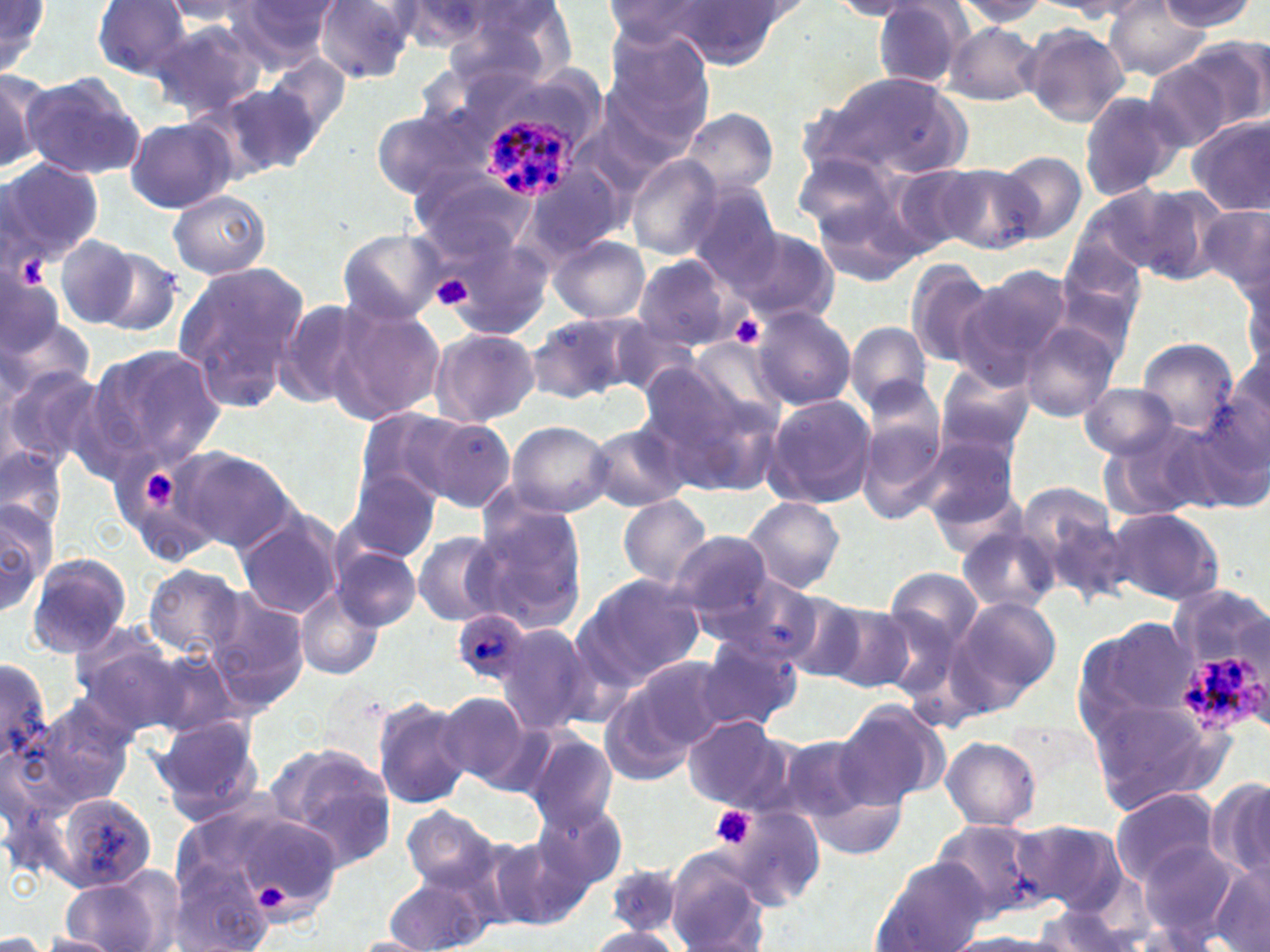
Approximate bounding boxes as (x1, y1, x2, y2) in pixels. Platelet locations: (432, 273, 473, 311), (729, 313, 766, 350), (132, 464, 189, 514), (709, 805, 757, 851), (250, 879, 293, 916). Uninfected red blood cell locations: (0, 0, 55, 81), (433, 0, 573, 90), (949, 0, 1052, 30), (1161, 0, 1258, 32), (91, 1, 196, 80), (222, 1, 341, 70), (314, 1, 418, 84), (830, 1, 930, 19), (1051, 1, 1160, 20), (160, 2, 266, 27), (602, 2, 721, 49), (654, 2, 793, 70), (869, 2, 975, 89), (391, 3, 495, 50), (1104, 3, 1212, 79), (150, 18, 268, 118), (941, 22, 1044, 105), (1020, 23, 1131, 125), (604, 32, 715, 145), (1173, 34, 1270, 139), (264, 54, 351, 141), (1141, 54, 1246, 152), (0, 68, 44, 175), (22, 70, 143, 180), (811, 71, 971, 180), (218, 82, 328, 176), (1077, 90, 1184, 202), (371, 107, 488, 201), (680, 108, 780, 198), (1188, 114, 1270, 216), (126, 117, 233, 213), (791, 150, 915, 255), (994, 151, 1087, 243), (626, 157, 726, 261), (1, 159, 103, 266), (935, 161, 1042, 255), (521, 164, 627, 265), (410, 168, 536, 257), (683, 182, 783, 287), (1110, 182, 1228, 287), (811, 183, 925, 288), (169, 189, 270, 278), (1199, 200, 1270, 295), (426, 221, 553, 336), (720, 222, 841, 326), (337, 228, 448, 325), (52, 233, 140, 329), (548, 235, 649, 324), (89, 245, 186, 337), (631, 254, 743, 351), (904, 258, 997, 368), (171, 262, 312, 413), (1241, 268, 1269, 374), (951, 273, 1068, 388), (273, 296, 379, 411), (326, 301, 447, 428), (0, 303, 94, 416), (750, 305, 855, 410), (526, 310, 646, 402), (604, 317, 708, 400), (845, 321, 933, 413), (1018, 322, 1121, 422), (430, 327, 540, 427), (678, 337, 789, 431), (1139, 338, 1237, 434), (89, 345, 227, 467), (934, 361, 1037, 459), (0, 362, 109, 478), (642, 370, 777, 492), (1078, 383, 1181, 460), (856, 388, 950, 523), (761, 394, 879, 510), (1191, 394, 1270, 506), (349, 410, 457, 518), (398, 411, 516, 510), (504, 420, 614, 516), (588, 422, 690, 513), (1103, 423, 1212, 520), (918, 434, 1022, 543), (1, 444, 66, 537), (172, 447, 295, 553), (341, 470, 444, 565), (1021, 485, 1128, 595), (618, 494, 714, 588), (0, 495, 55, 620), (741, 496, 844, 594), (472, 502, 588, 631), (1107, 507, 1226, 606), (234, 509, 346, 620), (956, 522, 1060, 614), (413, 531, 509, 627), (669, 531, 776, 625), (331, 547, 421, 633), (25, 553, 133, 658), (144, 565, 245, 658), (881, 566, 985, 658), (571, 572, 707, 689), (706, 572, 832, 670), (296, 584, 385, 681), (770, 588, 868, 683), (207, 590, 311, 713), (950, 595, 1060, 708), (821, 601, 915, 692), (1073, 614, 1200, 734), (493, 621, 592, 735), (69, 625, 184, 734), (693, 634, 802, 732), (139, 646, 247, 740), (622, 656, 734, 753), (0, 659, 56, 768), (596, 684, 701, 789), (434, 691, 537, 791), (371, 694, 473, 809), (27, 695, 136, 811), (1087, 696, 1232, 811), (837, 698, 951, 806), (680, 714, 796, 813), (151, 715, 264, 825), (779, 730, 892, 836), (523, 731, 619, 829), (940, 736, 1041, 831), (262, 742, 397, 874), (1208, 776, 1270, 885), (1109, 789, 1222, 887), (48, 790, 160, 894), (532, 799, 630, 893), (182, 800, 343, 931), (399, 805, 504, 894), (724, 805, 825, 908), (930, 818, 1053, 920), (1012, 820, 1127, 913), (488, 839, 590, 930), (1136, 841, 1242, 945), (665, 854, 772, 952), (869, 860, 992, 952), (167, 863, 274, 952), (1208, 864, 1270, 952), (604, 866, 687, 940), (380, 867, 498, 952), (57, 870, 172, 952), (1030, 905, 1141, 951), (583, 928, 685, 951), (0, 929, 45, 952), (38, 932, 121, 951), (947, 932, 1069, 951), (347, 935, 437, 951). Plasmodium ovale-infected red blood cell locations: (482, 114, 581, 204), (453, 608, 532, 685), (1175, 646, 1263, 736). Slide-level diagnosis: Plasmodium ovale. Single field of view. May-Grünwald-Giemsa stain. Thin blood film. 1000x magnification. Optical microscopy. Image is 1270×952 pixels.